Identify the preparation type.
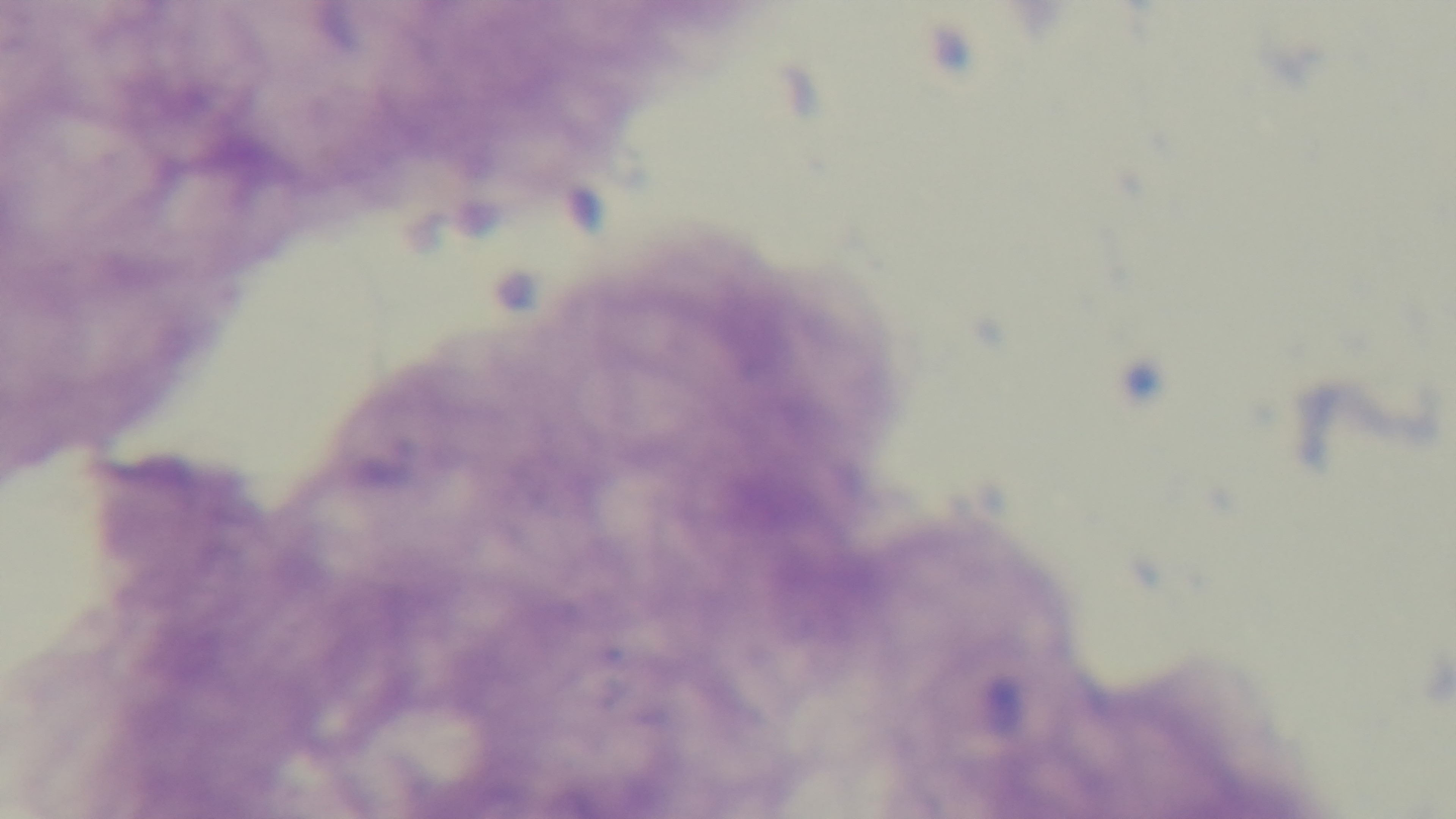

Thick.

field of view = one from the slide
modality = light microscopy
capture = mounted 4K digital camera
objective = 100x oil immersion
stain = Giemsa
malaria status = negative